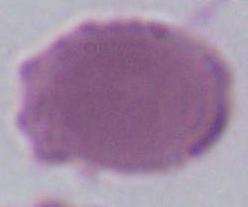

Summary:
  - Identification: erythrocyte
  - Magnification: 1000x
  - Modality: photomicrograph